Mark where platelets are.
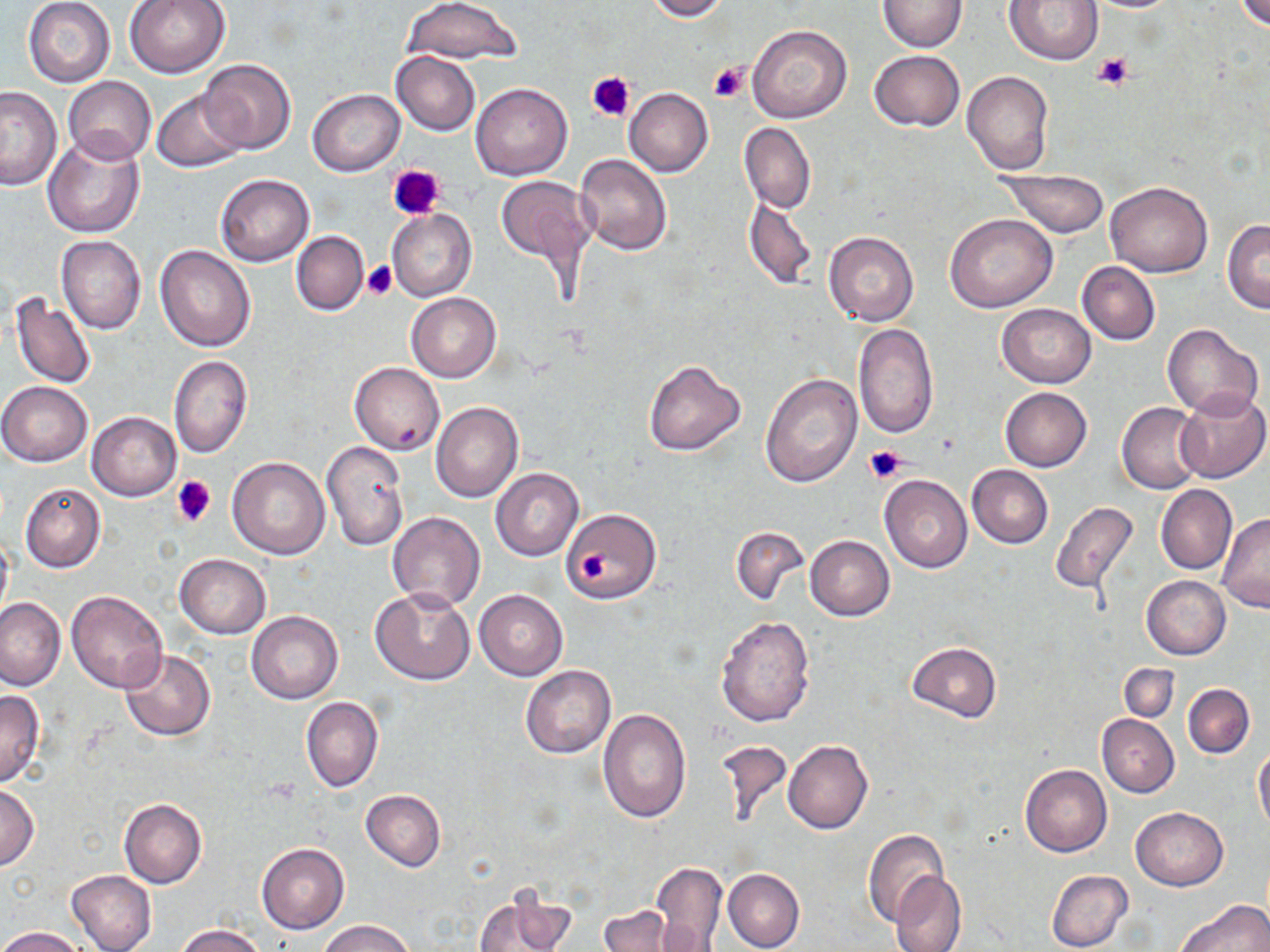

Approximate bounding boxes as (x1, y1, x2, y2) in pixels.
Platelets: (1091, 51, 1136, 90), (708, 61, 749, 102), (585, 70, 634, 124), (387, 163, 445, 219), (363, 262, 396, 299), (864, 444, 906, 482), (171, 474, 216, 527), (579, 550, 609, 581).

Uninfected red blood cell locations: (124, 0, 232, 78), (402, 0, 523, 66), (645, 0, 730, 21), (1004, 0, 1105, 66), (1235, 0, 1270, 29), (23, 1, 115, 87), (878, 1, 967, 51), (747, 24, 852, 124), (869, 50, 964, 132), (391, 51, 480, 135), (197, 59, 297, 155), (963, 71, 1053, 174), (62, 75, 156, 166), (470, 81, 573, 180), (0, 87, 63, 190), (308, 88, 404, 175), (624, 88, 713, 177), (152, 89, 248, 172), (739, 123, 816, 215), (42, 132, 144, 238), (575, 153, 672, 255), (996, 167, 1111, 239), (215, 174, 314, 266), (494, 176, 597, 271), (1106, 180, 1213, 277), (743, 194, 815, 288), (386, 208, 476, 303), (946, 213, 1057, 313), (1223, 219, 1270, 312), (292, 231, 369, 315), (822, 232, 919, 326), (56, 235, 146, 335), (155, 243, 256, 352), (1077, 261, 1160, 345), (9, 291, 96, 391), (407, 293, 501, 382), (996, 303, 1095, 388), (852, 323, 939, 440), (1163, 323, 1264, 420), (168, 355, 253, 459), (642, 360, 745, 456), (349, 361, 444, 456), (760, 373, 862, 487), (0, 382, 92, 466), (1000, 387, 1091, 471), (1175, 388, 1270, 484), (433, 402, 524, 502), (1116, 402, 1205, 494), (87, 411, 181, 500), (321, 440, 409, 551), (228, 456, 330, 560), (967, 464, 1053, 547), (490, 467, 584, 561), (880, 475, 972, 573), (20, 481, 106, 573), (1155, 485, 1237, 575), (1049, 501, 1139, 596), (560, 508, 661, 602), (388, 512, 486, 609), (1218, 513, 1269, 613), (730, 527, 809, 607), (0, 528, 13, 628), (805, 535, 895, 621), (174, 554, 271, 639), (1142, 575, 1231, 660), (370, 588, 476, 686), (67, 589, 169, 693), (475, 590, 567, 680), (0, 597, 66, 691), (246, 610, 343, 704), (716, 615, 816, 728), (907, 641, 1001, 722), (119, 649, 216, 741), (1119, 664, 1178, 722), (521, 665, 615, 759), (1182, 683, 1255, 758), (0, 690, 44, 786), (301, 696, 383, 793), (597, 709, 691, 823), (1097, 714, 1179, 797), (713, 736, 793, 832), (783, 741, 874, 834), (1253, 744, 1270, 833), (1020, 764, 1112, 857), (0, 785, 40, 870), (360, 789, 446, 871), (119, 798, 207, 889), (1130, 808, 1228, 891), (863, 829, 952, 928), (257, 843, 349, 933), (649, 861, 727, 952), (724, 868, 805, 952), (1046, 869, 1133, 952), (67, 870, 157, 952), (889, 870, 967, 952), (474, 887, 577, 952), (1178, 899, 1269, 951), (598, 905, 687, 952), (319, 920, 414, 952), (175, 923, 267, 952), (0, 926, 88, 952). Slide-level diagnosis: no evidence of blood parasites. May-Grünwald-Giemsa-stained preparation. Thin blood smear. Light microscopy. One field of a larger specimen. 1000x magnification. Image is 1270×952 pixels.